Assess for Plasmodium parasites.
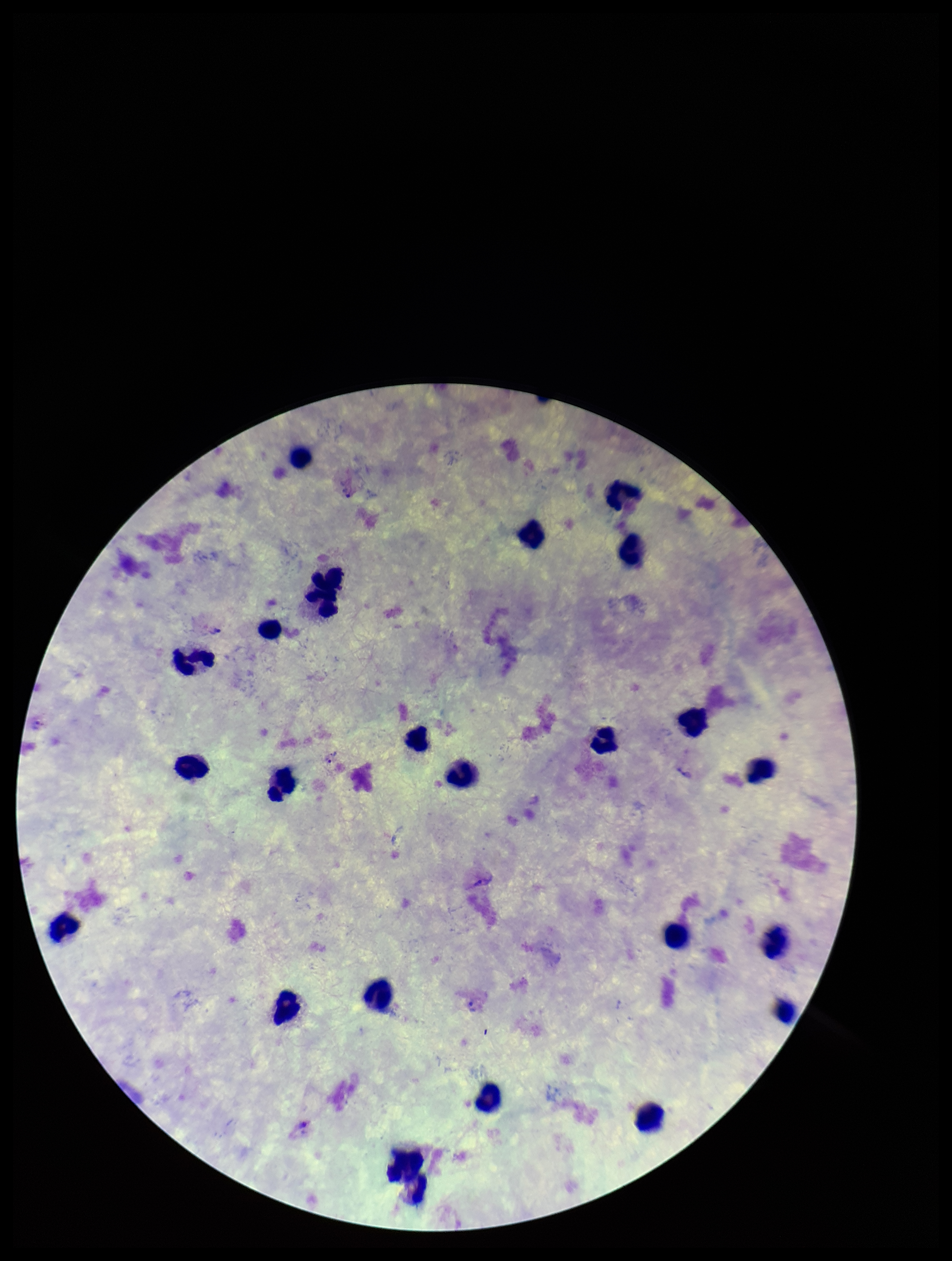
Seen.

image_size: 952×1261 pixels
parasite_count: 2
species_reported_for_this_patient: Plasmodium vivax
leukocyte_count: 22
patient_malaria_status: infected
field_of_view: single
stain: Giemsa
preparation: thick smear
capture: smartphone photograph through the microscope eyepiece